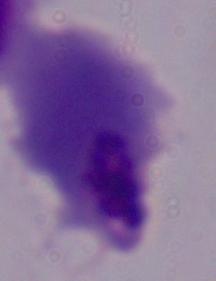

modality = micrograph
magnification = 1000x
identification = trichomonad